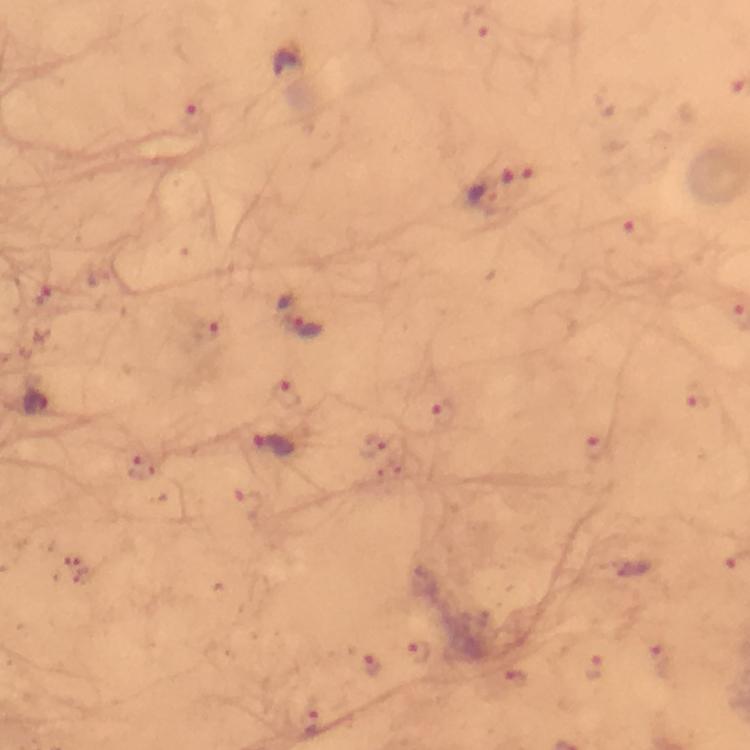

Approximate centers as [x, y] in pixels.
Summary:
  - Malaria parasite locations: [518, 173], [482, 197], [302, 326], [696, 399], [36, 402], [274, 446], [595, 447], [419, 653], [373, 667], [594, 667]
  - Preparation: thick smear
  - Stain: Giemsa
  - Magnification: 100x
  - Cropped from: a single field of view
  - Image size: 750×750 pixels
  - Capture: smartphone camera through the microscope
  - Immersion oil: applied
  - Context: from a diagnostic examination for malaria